Assess this cell for malaria.
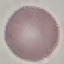

It is uninfected.

Summary:
  - Preparation: thin smear
  - Image type: automatically extracted cell patch, resized to 64 × 64 pixels
  - Capture: smartphone through the microscope eyepiece
  - Stain: Giemsa